Report the malaria status of this cell.
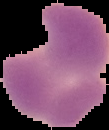
It is parasitized.

Image is 109×130 pixels. From a thin blood smear. Segmented cell region on a black background.